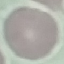

result: no malaria parasites seen
stain: Giemsa
image_type: automatically extracted cell patch, resized to 64 × 64 pixels
preparation: thin blood smear
capture: smartphone camera at the microscope eyepiece